Describe the morphology of the red blood cells.
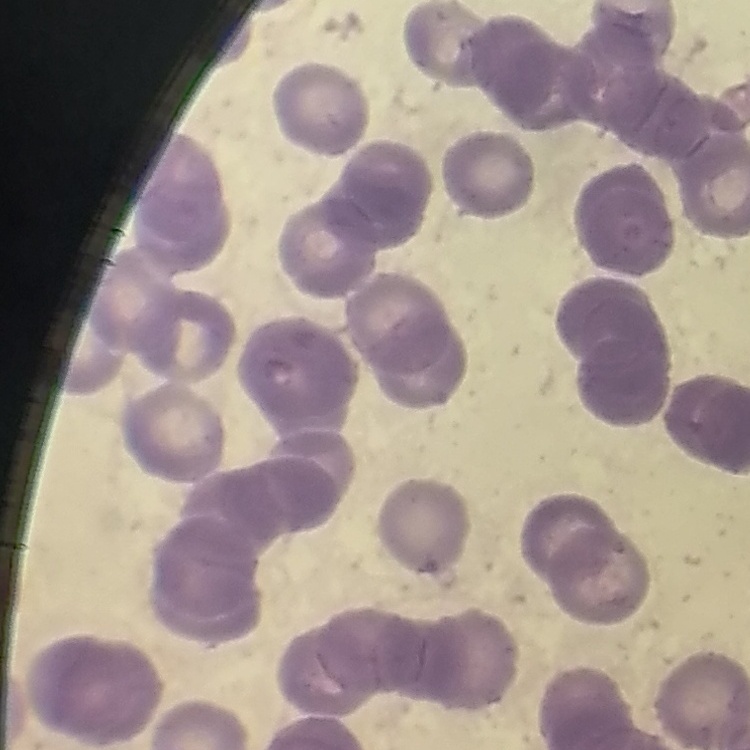

Rouleaux formation.

{
  "preparation": "thin blood smear",
  "image_type": "square crop of a larger photomicrograph",
  "stain": "Field's or Giemsa"
}